Describe the morphology of the erythrocytes.
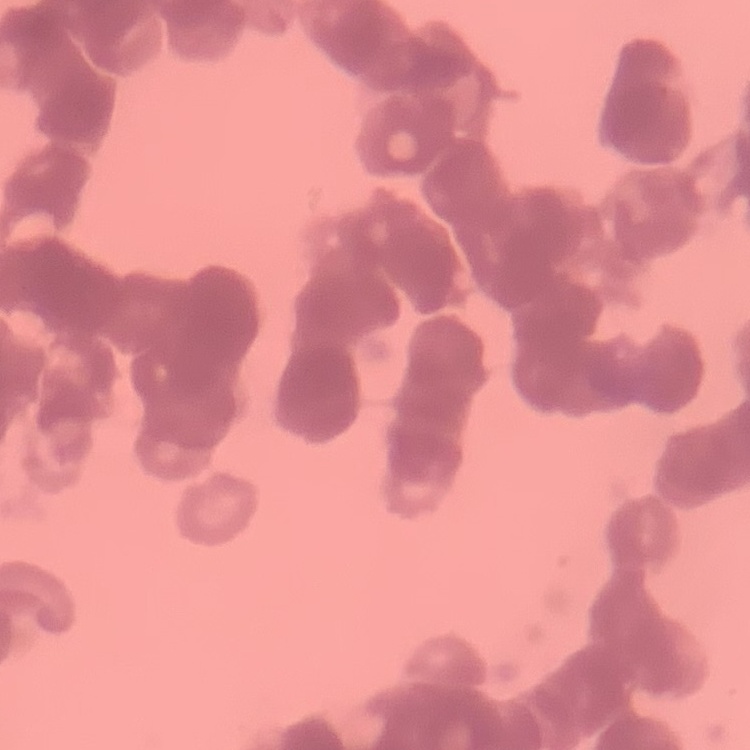

Rouleaux formation.

One tile cut from a larger photomicrograph. Field's or Giemsa stain. Thin blood smear.